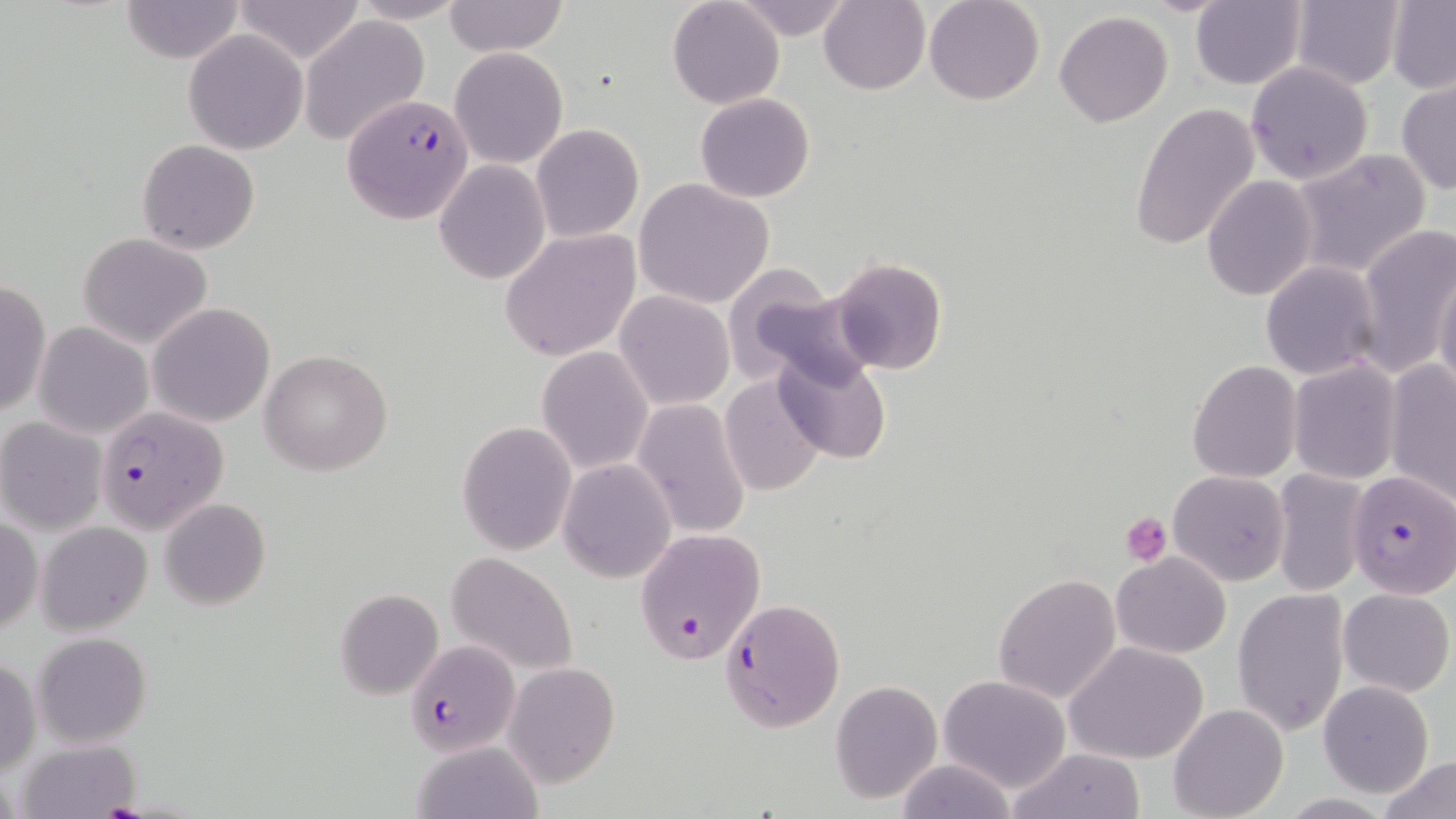
Approximate bounding boxes as [x1, y1, x2, y2] in pixels. Plasmodium falciparum-infected red blood cell locations: [339, 95, 474, 226], [94, 404, 229, 533], [1347, 470, 1455, 597], [634, 527, 765, 665], [721, 598, 846, 731], [406, 641, 520, 757]. Platelet locations: [1121, 511, 1173, 565], [97, 800, 149, 817]. Uninfected red blood cell locations: [120, 0, 246, 64], [232, 0, 367, 66], [347, 0, 471, 24], [818, 0, 930, 95], [924, 0, 1045, 105], [1190, 0, 1307, 90], [443, 1, 568, 57], [666, 1, 785, 110], [731, 1, 857, 42], [1289, 1, 1404, 88], [1386, 2, 1456, 91], [1054, 11, 1173, 127], [299, 16, 431, 144], [184, 31, 307, 153], [449, 46, 568, 169], [1246, 62, 1374, 186], [1395, 78, 1456, 196], [695, 92, 815, 203], [1130, 103, 1261, 253], [531, 123, 644, 243], [136, 139, 258, 254], [1287, 148, 1433, 280], [434, 160, 551, 285], [1203, 175, 1318, 301], [633, 178, 774, 309], [1353, 221, 1456, 380], [499, 227, 642, 363], [77, 231, 215, 350], [827, 255, 949, 376], [1259, 260, 1383, 381], [1433, 266, 1456, 396], [725, 267, 862, 387], [0, 277, 49, 418], [612, 290, 734, 410], [146, 303, 276, 427], [33, 322, 153, 439], [536, 346, 653, 474], [260, 348, 393, 477], [773, 351, 894, 466], [1286, 359, 1402, 485], [1187, 360, 1303, 482], [1383, 360, 1456, 507], [720, 372, 828, 496], [633, 398, 753, 539], [0, 416, 109, 535], [456, 421, 576, 555], [556, 458, 674, 584], [1272, 468, 1370, 597], [1168, 470, 1291, 585], [159, 498, 271, 610], [0, 515, 43, 638], [36, 521, 153, 637], [447, 552, 578, 676], [1111, 552, 1231, 658], [473, 571, 603, 765], [992, 572, 1121, 705], [1232, 587, 1350, 736], [1338, 587, 1454, 696], [334, 588, 443, 698], [32, 632, 153, 749], [1065, 640, 1211, 766], [0, 657, 40, 779], [503, 662, 619, 787], [938, 675, 1070, 792], [831, 679, 941, 804], [1318, 680, 1435, 798], [1170, 702, 1289, 819], [13, 738, 144, 818], [410, 739, 544, 819], [1007, 747, 1146, 819], [1378, 754, 1456, 819], [894, 757, 1020, 819]. Slide-level diagnosis: Plasmodium falciparum. Thin blood smear. May-Grünwald-Giemsa-stained preparation. Captured at 1000x magnification. Optical microscopy. One field of a larger specimen. Image is 1456×819 pixels.